Point out each malaria parasite.
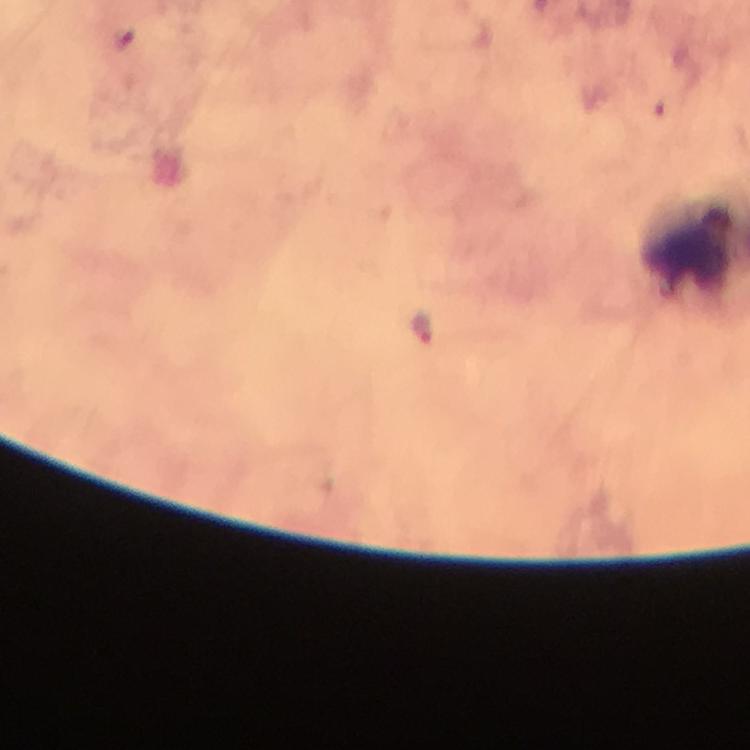
Approximate object centers, in pixels from the top-left corner.
Malaria parasites: (x=423, y=329).

Image is 750×750 pixels. Immersion oil applied. Smartphone photograph taken through a microscope. At 100x magnification. Giemsa stain. Thick blood smear. Cropped region of a single field of view. From a diagnostic examination for malaria.